Comment on the morphology of the erythrocytes.
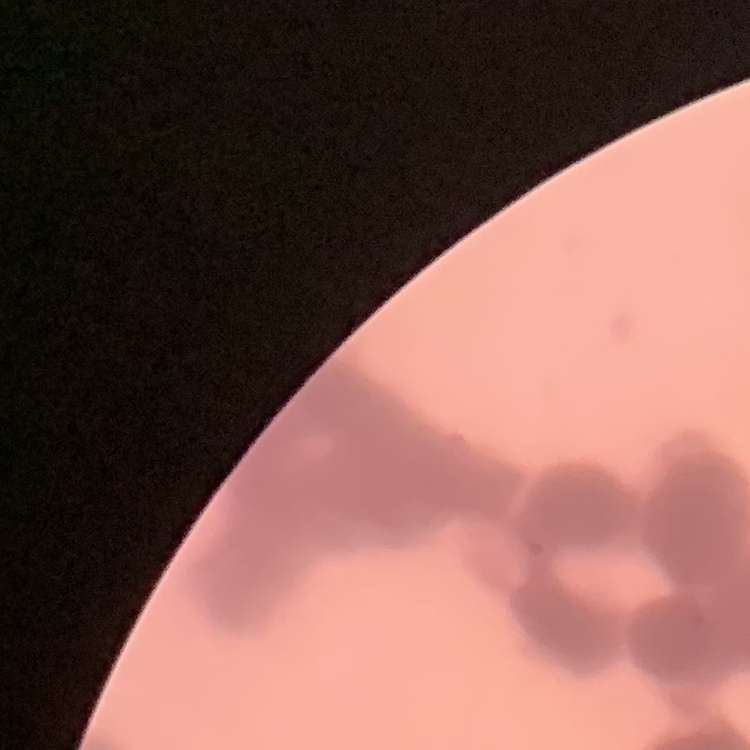
Rouleaux formation.

Field's or Giemsa stain. Square crop of a larger photomicrograph. Thin peripheral smear.